Assess this cell for malaria.
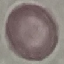

Uninfected.

capture = smartphone through the microscope eyepiece
image type = automatically extracted cell patch, resized to 64 × 64 pixels
preparation = thin smear
stain = Giemsa